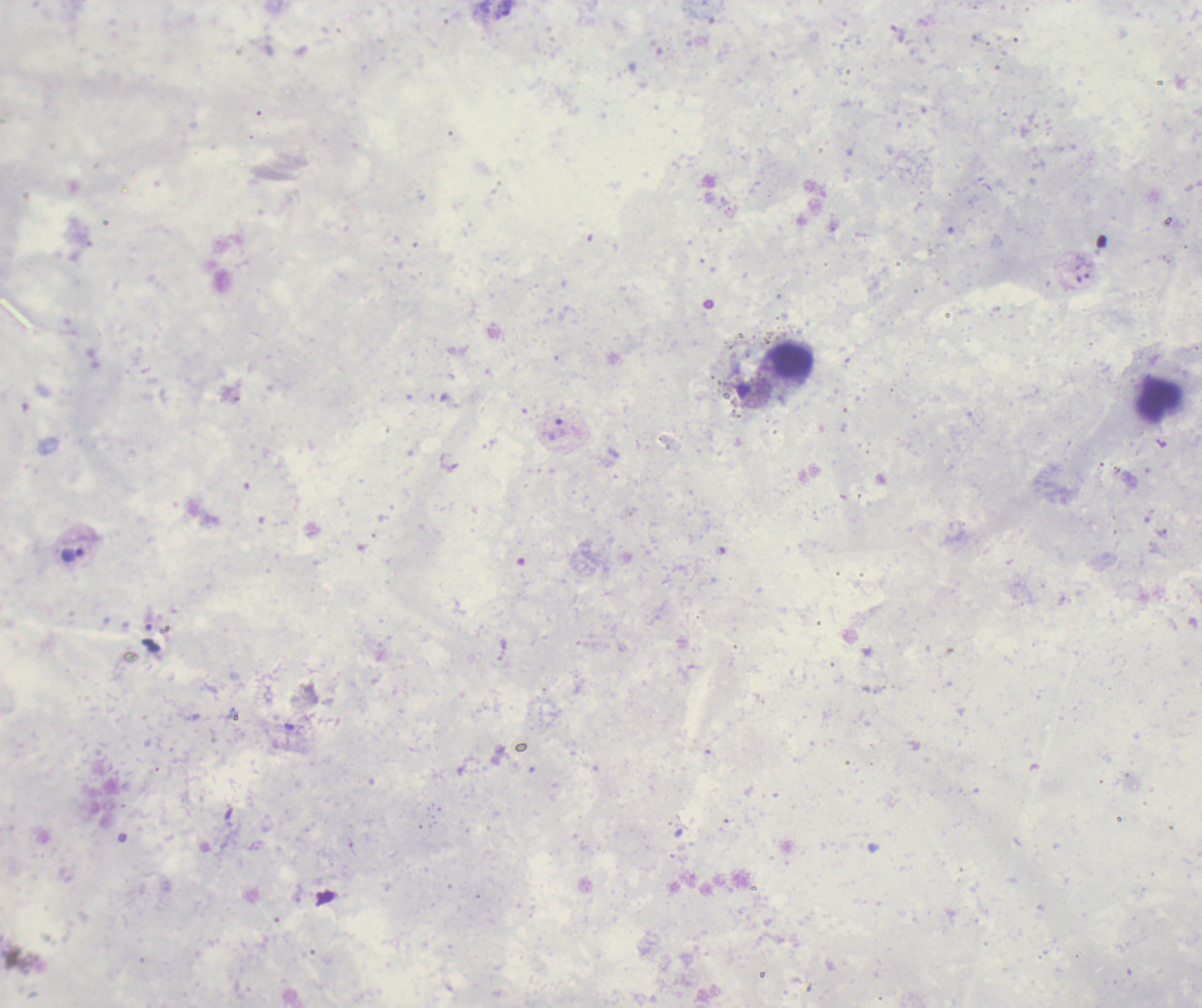 Approximate object centers, in pixels from the top-left corner. Trophozoite locations: (x=507, y=8), (x=1087, y=269), (x=557, y=430), (x=72, y=554). Leukocyte locations: (x=793, y=362). Romanowsky-stained preparation. 100x magnification. Result: Plasmodium parasites detected. Previously used in an actual diagnosis. Single field of view. Background quality: unsatisfactory. Image is 1202×1008 pixels. Thick blood film.